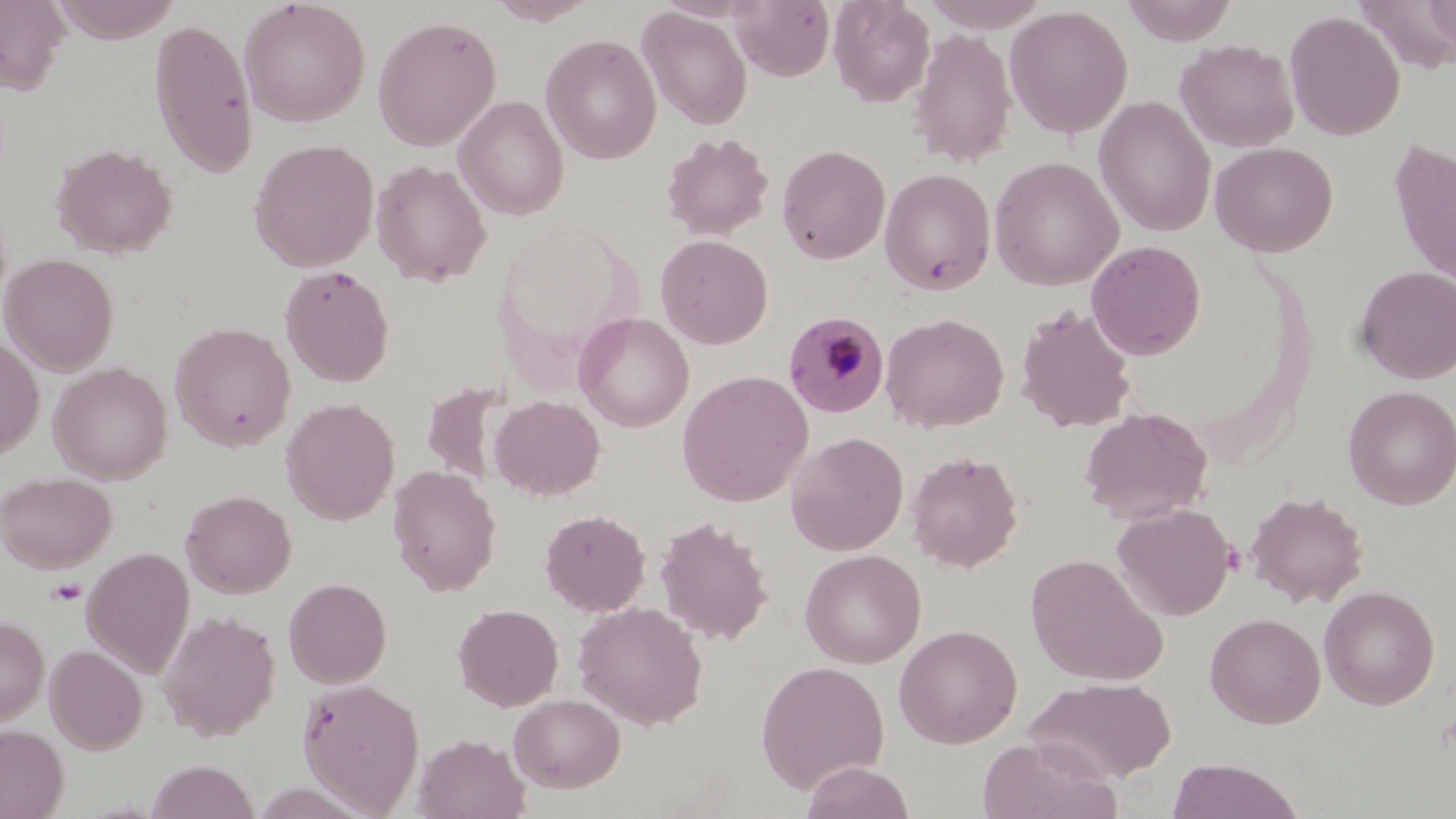
Summary:
  - Coordinate format: approximate bounding boxes as (x1, y1, x2, y2) in pixels
  - Plasmodium malariae-infected red blood cell locations: (783, 310, 890, 418)
  - Platelet locations: (46, 578, 87, 606)
  - Uninfected red blood cell locations: (0, 0, 70, 95), (47, 0, 183, 42), (487, 0, 600, 25), (732, 0, 835, 82), (828, 0, 935, 107), (919, 0, 1051, 31), (1120, 0, 1239, 45), (1422, 0, 1455, 46), (239, 1, 371, 127), (1356, 2, 1456, 69), (1004, 5, 1133, 138), (638, 7, 753, 130), (1285, 10, 1405, 141), (372, 14, 502, 151), (149, 17, 259, 179), (908, 28, 1016, 167), (540, 33, 661, 164), (1175, 38, 1299, 153), (454, 95, 569, 219), (1094, 96, 1216, 237), (661, 132, 774, 241), (1388, 137, 1456, 294), (248, 138, 380, 271), (1210, 141, 1338, 257), (51, 142, 178, 258), (776, 144, 891, 264), (989, 156, 1123, 290), (371, 160, 491, 286), (880, 168, 996, 295), (656, 234, 773, 349), (1085, 240, 1206, 360), (1, 253, 120, 375), (279, 265, 394, 387), (1356, 265, 1456, 384), (1015, 304, 1137, 432), (574, 312, 694, 432), (880, 312, 1009, 432), (170, 321, 296, 451), (0, 334, 44, 459), (49, 361, 173, 485), (677, 370, 814, 506), (420, 380, 508, 489), (1343, 385, 1456, 510), (490, 394, 605, 499), (281, 398, 400, 525), (1080, 407, 1213, 525), (786, 432, 909, 556), (906, 450, 1023, 571), (387, 465, 501, 595), (0, 472, 117, 573), (181, 490, 297, 599), (1246, 490, 1368, 607), (1113, 503, 1236, 621), (540, 509, 651, 617), (655, 515, 773, 645), (81, 547, 195, 677), (800, 549, 926, 668), (1025, 553, 1168, 686), (283, 578, 393, 688), (1318, 585, 1440, 710), (573, 601, 708, 729), (453, 604, 564, 711), (160, 610, 280, 740), (1206, 612, 1326, 728), (0, 616, 49, 727), (894, 624, 1023, 748), (45, 644, 148, 754), (755, 660, 890, 792), (1025, 676, 1176, 784), (297, 677, 425, 815), (508, 693, 626, 793), (0, 724, 68, 819), (412, 733, 530, 819), (978, 738, 1121, 819), (1166, 758, 1305, 819), (146, 759, 261, 819), (800, 761, 916, 819)
  - Slide-level diagnosis: Plasmodium malariae
  - Field of view: one of a larger specimen
  - Preparation: thin blood film
  - Stain: May-Grünwald-Giemsa
  - Magnification: 1000x
  - Image size: 1456×819 pixels
  - Modality: optical microscopy